Name the parasite shown.
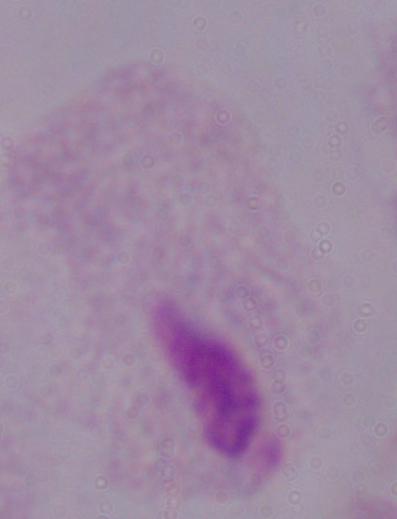
This is a trichomonad.

Captured at 1000x magnification. Photomicrograph.